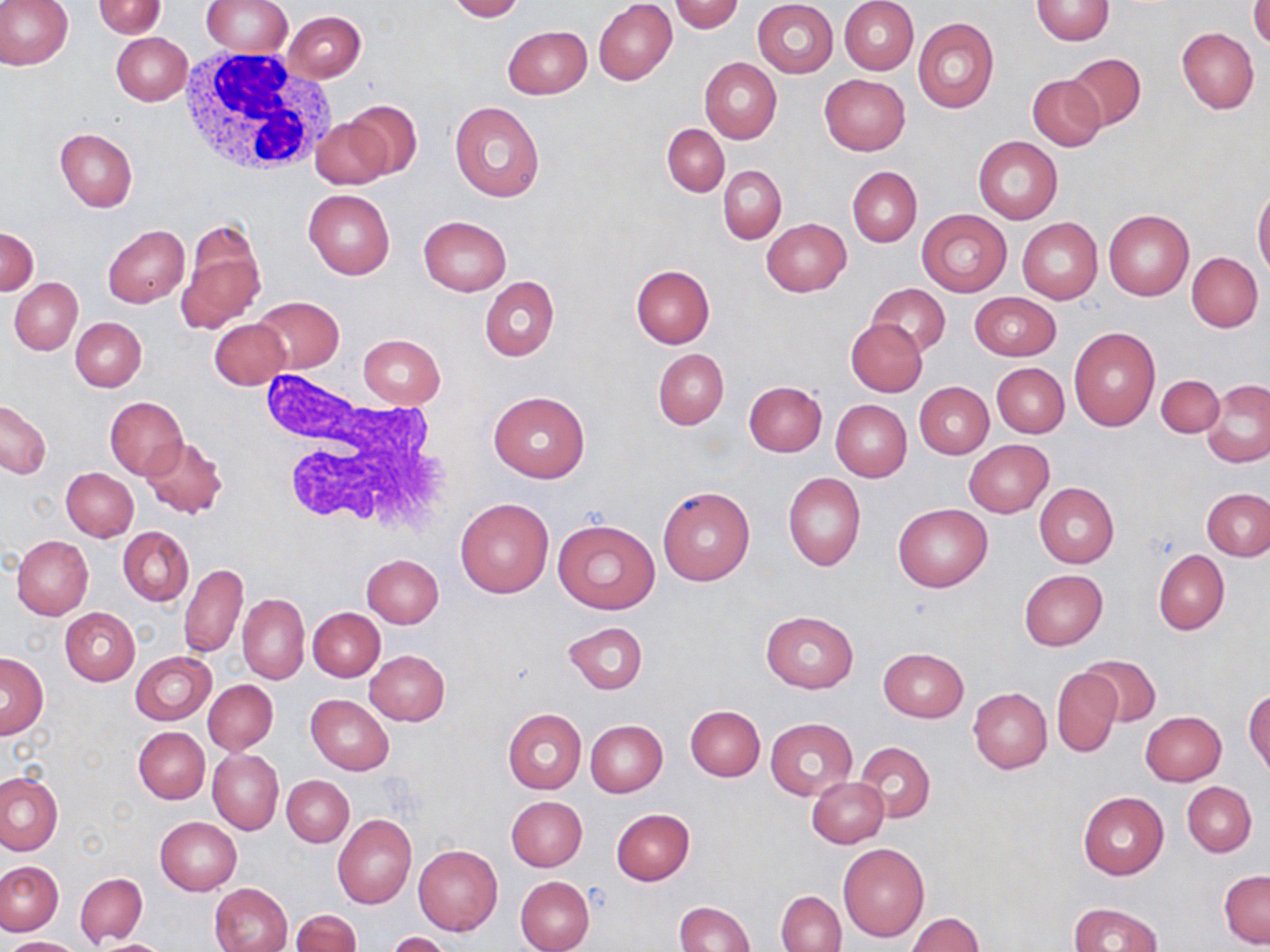

slide-level diagnosis = negative for blood parasites
preparation = thin blood smear
modality = optical microscopy
white blood cell locations = approximate bounding boxes as [x1, y1, x2, y2] in pixels: [176, 47, 333, 177], [260, 369, 451, 538]
uninfected red blood cell locations = approximate bounding boxes as [x1, y1, x2, y2] in pixels: [0, 0, 72, 71], [201, 0, 292, 57], [840, 0, 918, 74], [1030, 0, 1114, 45], [92, 1, 166, 38], [446, 1, 524, 22], [594, 1, 678, 85], [668, 1, 744, 34], [753, 1, 838, 77], [1249, 1, 1270, 49], [283, 11, 366, 82], [913, 18, 999, 115], [503, 25, 591, 99], [1176, 26, 1259, 113], [111, 32, 192, 106], [1062, 52, 1145, 131], [699, 58, 782, 143], [818, 74, 910, 156], [1028, 74, 1107, 151], [345, 100, 422, 178], [449, 101, 546, 202], [312, 117, 393, 190], [662, 123, 729, 196], [55, 129, 138, 211], [974, 136, 1063, 223], [719, 164, 786, 244], [847, 166, 921, 247], [1253, 186, 1270, 280], [303, 189, 395, 278], [1103, 210, 1193, 301], [918, 211, 1011, 295], [418, 215, 511, 295], [177, 217, 266, 335], [1017, 217, 1102, 304], [762, 218, 850, 296], [103, 225, 189, 308], [1, 227, 38, 294], [1187, 251, 1264, 331], [630, 265, 714, 349], [480, 277, 559, 361], [9, 278, 82, 355], [866, 283, 950, 357], [969, 293, 1061, 360], [252, 295, 344, 374], [70, 317, 146, 391], [846, 317, 927, 396], [211, 319, 290, 390], [1068, 327, 1160, 430], [357, 334, 445, 409], [653, 348, 729, 430], [992, 363, 1068, 438], [1157, 374, 1224, 438], [1202, 378, 1270, 467], [743, 380, 827, 456], [915, 381, 993, 458], [489, 392, 589, 482], [105, 397, 188, 479], [0, 399, 53, 478], [830, 399, 911, 481], [141, 437, 229, 519], [963, 440, 1054, 518], [62, 467, 137, 541], [783, 472, 866, 571], [1034, 483, 1118, 567], [657, 486, 755, 584], [1202, 487, 1270, 561], [456, 498, 553, 598], [892, 502, 992, 593], [553, 519, 661, 614], [118, 527, 193, 605], [12, 534, 93, 620], [1154, 550, 1229, 634], [361, 554, 443, 628], [180, 563, 248, 658], [1019, 569, 1108, 650], [237, 593, 309, 685], [60, 607, 139, 686], [308, 608, 385, 682], [761, 610, 858, 692], [562, 621, 647, 694], [878, 647, 968, 723], [366, 650, 449, 725], [130, 651, 216, 725], [0, 652, 48, 738], [1080, 654, 1161, 728], [1051, 667, 1122, 757], [204, 680, 278, 754], [969, 688, 1051, 773], [1245, 688, 1269, 777], [307, 694, 395, 775], [685, 704, 764, 781], [503, 708, 586, 794], [1140, 711, 1226, 786], [765, 718, 857, 800], [584, 720, 667, 796], [133, 726, 209, 804], [854, 741, 935, 823], [208, 749, 283, 834], [0, 772, 64, 855], [282, 775, 353, 847], [806, 776, 888, 848], [1182, 782, 1256, 856], [1078, 792, 1168, 880], [505, 795, 587, 872], [611, 809, 695, 885], [333, 813, 416, 909], [155, 817, 241, 895], [838, 843, 930, 942], [414, 844, 502, 935], [0, 861, 64, 936], [1220, 869, 1269, 948], [76, 873, 147, 946], [515, 876, 594, 952], [208, 882, 292, 952], [776, 890, 846, 952], [673, 901, 755, 952], [1068, 902, 1162, 952], [290, 910, 360, 952], [908, 913, 984, 951], [386, 932, 453, 952], [5, 936, 81, 951], [87, 938, 174, 952]
stain = May-Grünwald-Giemsa
image size = 1270×952 pixels
field of view = single
magnification = 1000x